Look for parasitized red blood cells.
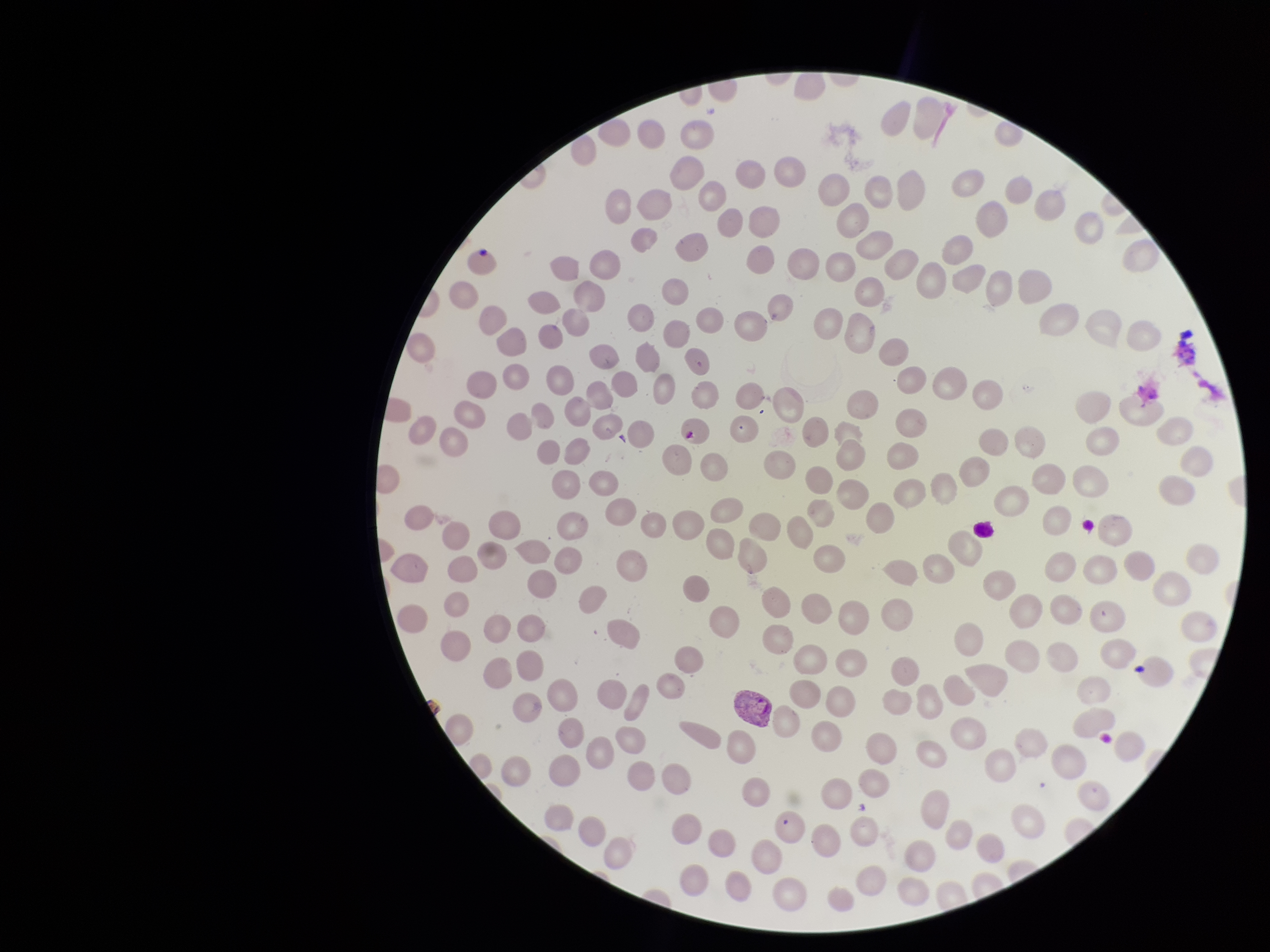

Identified.

Summary:
  - Preparation: thin smear
  - Patient malaria status: infected
  - Field of view: single
  - Parasitized red blood cell count: 1
  - Capture: smartphone photograph through the microscope eyepiece
  - Species reported for this patient: Plasmodium vivax
  - Stain: Giemsa
  - Red blood cell count: 200
  - Image size: 1270×952 pixels